Outline each uninfected red blood cell.
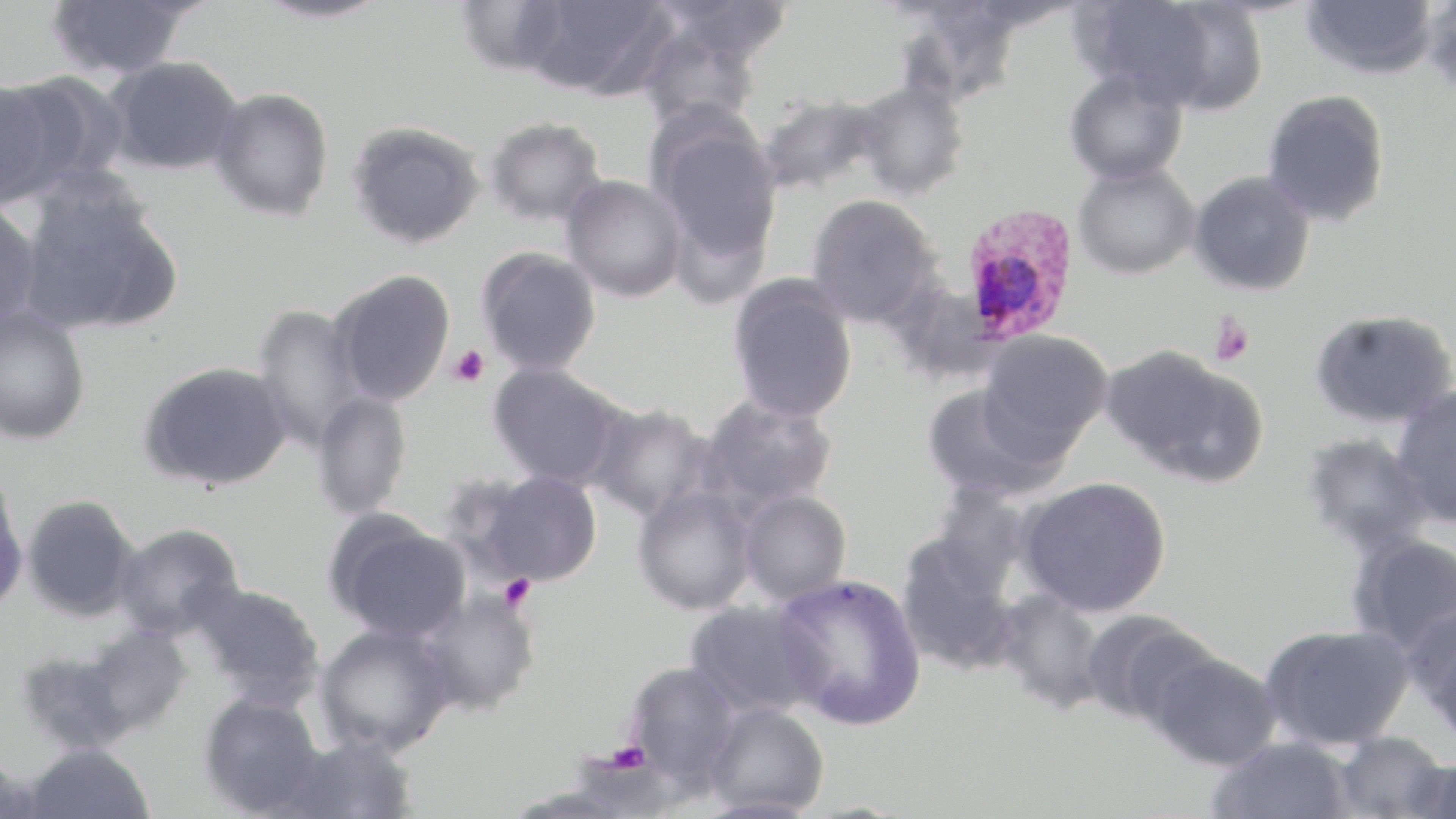
Approximate bounding boxes as (x1,y1)-(x2,y2) corner pairs in pixels.
Uninfected red blood cells: (252,0)-(392,25), (454,0)-(573,78), (651,0)-(796,65), (1072,0)-(1235,110), (1300,0)-(1440,80), (1419,0)-(1456,98), (46,1)-(196,80), (523,1)-(678,100), (891,3)-(1025,108), (636,18)-(767,133), (106,55)-(243,175), (1063,67)-(1189,186), (0,77)-(78,209), (852,80)-(971,200), (210,87)-(334,221), (1261,89)-(1391,228), (757,93)-(888,196), (647,115)-(783,266), (483,116)-(608,228), (347,121)-(487,250), (1073,162)-(1200,280), (1188,170)-(1316,296), (559,174)-(687,302), (17,178)-(183,336), (805,194)-(942,329), (0,199)-(42,334), (476,246)-(602,376), (330,269)-(456,407), (727,274)-(859,424), (886,279)-(1002,386), (252,304)-(368,450), (0,308)-(91,445), (1310,308)-(1456,429), (979,329)-(1114,449), (1102,345)-(1268,487), (139,360)-(293,492), (487,362)-(625,489), (920,381)-(1067,504), (1391,386)-(1456,529), (311,390)-(413,520), (696,395)-(839,514), (584,401)-(717,523), (1300,432)-(1434,556), (0,469)-(28,616), (465,469)-(604,588), (1016,476)-(1172,617), (632,484)-(758,615), (925,488)-(1032,599), (738,490)-(852,606), (22,495)-(139,621), (324,512)-(471,640), (113,523)-(245,641), (1346,531)-(1456,657), (895,535)-(1023,675), (772,573)-(927,730), (191,582)-(325,709), (994,589)-(1108,713), (417,590)-(540,716), (684,599)-(828,718), (1407,605)-(1456,744), (1079,609)-(1215,727), (315,623)-(454,756), (1259,624)-(1414,750), (76,626)-(192,737), (14,644)-(141,754), (1141,646)-(1282,771), (624,661)-(743,790), (198,691)-(324,816), (703,701)-(829,816), (1331,731)-(1449,818), (276,733)-(417,819), (1205,735)-(1355,819), (22,741)-(156,818), (0,754)-(43,818), (1401,757)-(1456,819).

Platelet locations: (1208,312)-(1255,366), (449,345)-(490,387), (499,574)-(537,612), (604,740)-(652,773). Plasmodium ovale-infected red blood cell locations: (958,205)-(1080,346). Slide-level diagnosis: Plasmodium ovale. Thin blood film. Captured at 1000x magnification. Optical microscopy. One field of a larger specimen. Image is 1456×819 pixels. May-Grünwald-Giemsa-stained preparation.